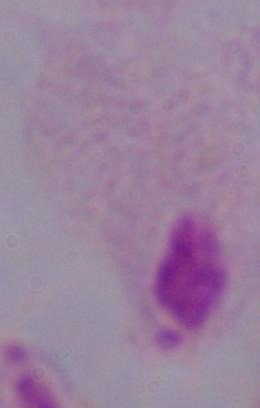
A trichomonad is shown. Captured at 1000x magnification. Micrograph.